Assess this cell for malaria.
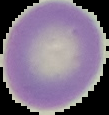

Uninfected.

image type = segmented cell region on a black background
preparation = thin blood smear
image size = 109×115 pixels